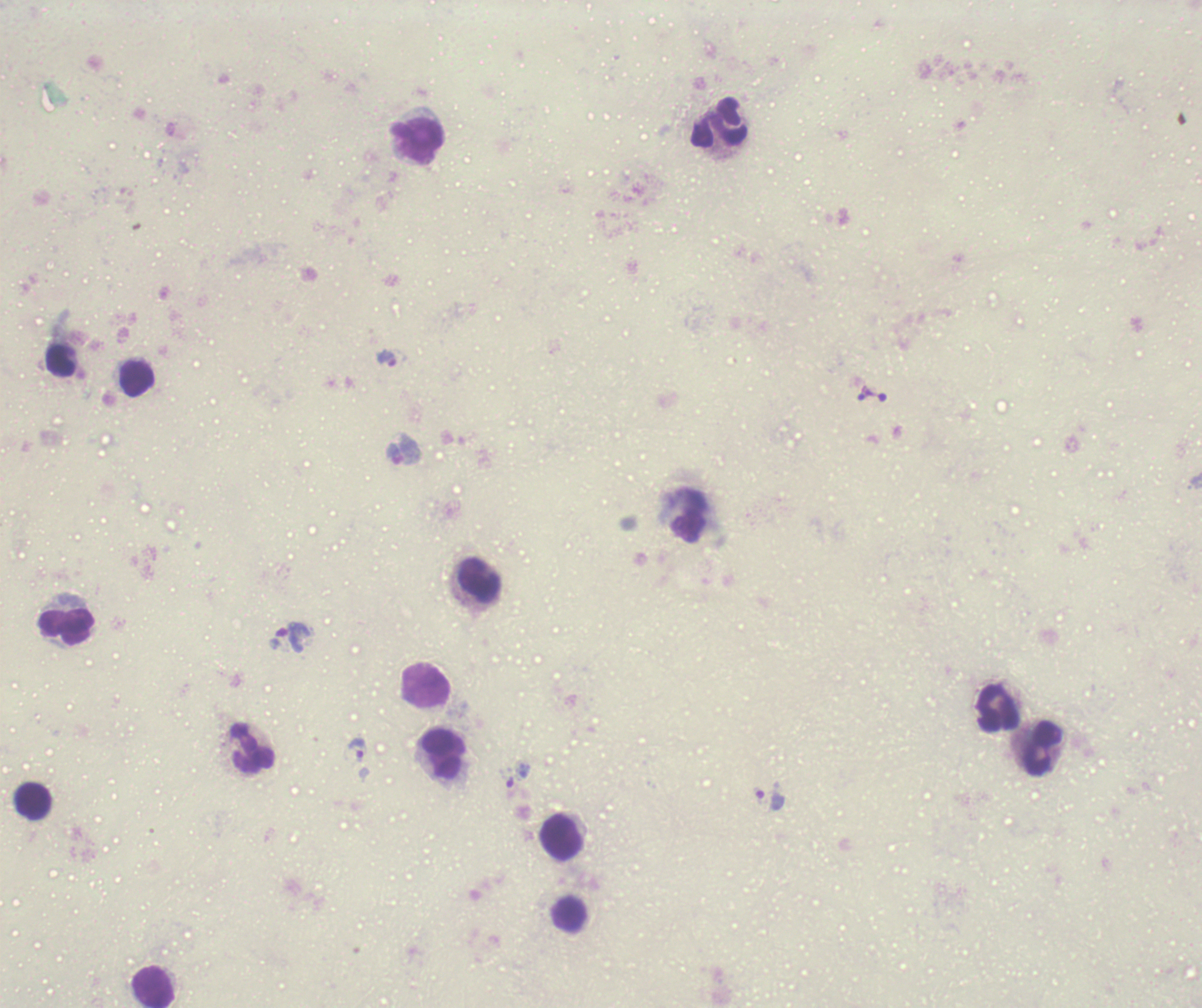

Approximate centers as {x, y} in pixels.
Summary:
  - Leukocyte locations: {719, 123}, {419, 142}, {61, 361}, {137, 379}, {689, 515}, {479, 580}, {67, 627}, {426, 685}, {998, 708}, {253, 748}, {1044, 749}, {444, 755}, {33, 801}, {562, 837}, {568, 915}, {153, 987}
  - Trophozoite locations: {387, 359}, {864, 392}, {404, 451}, {293, 637}, {359, 748}, {518, 776}, {770, 800}
  - Magnification: 100x
  - Image size: 1202×1008 pixels
  - Preparation: thick blood film
  - Context: previously used in an actual diagnosis
  - Background quality: unsatisfactory
  - Stain: Romanowsky
  - Field of view: one from this slide
  - Coloration quality: bad
  - Result: positive for malaria parasites